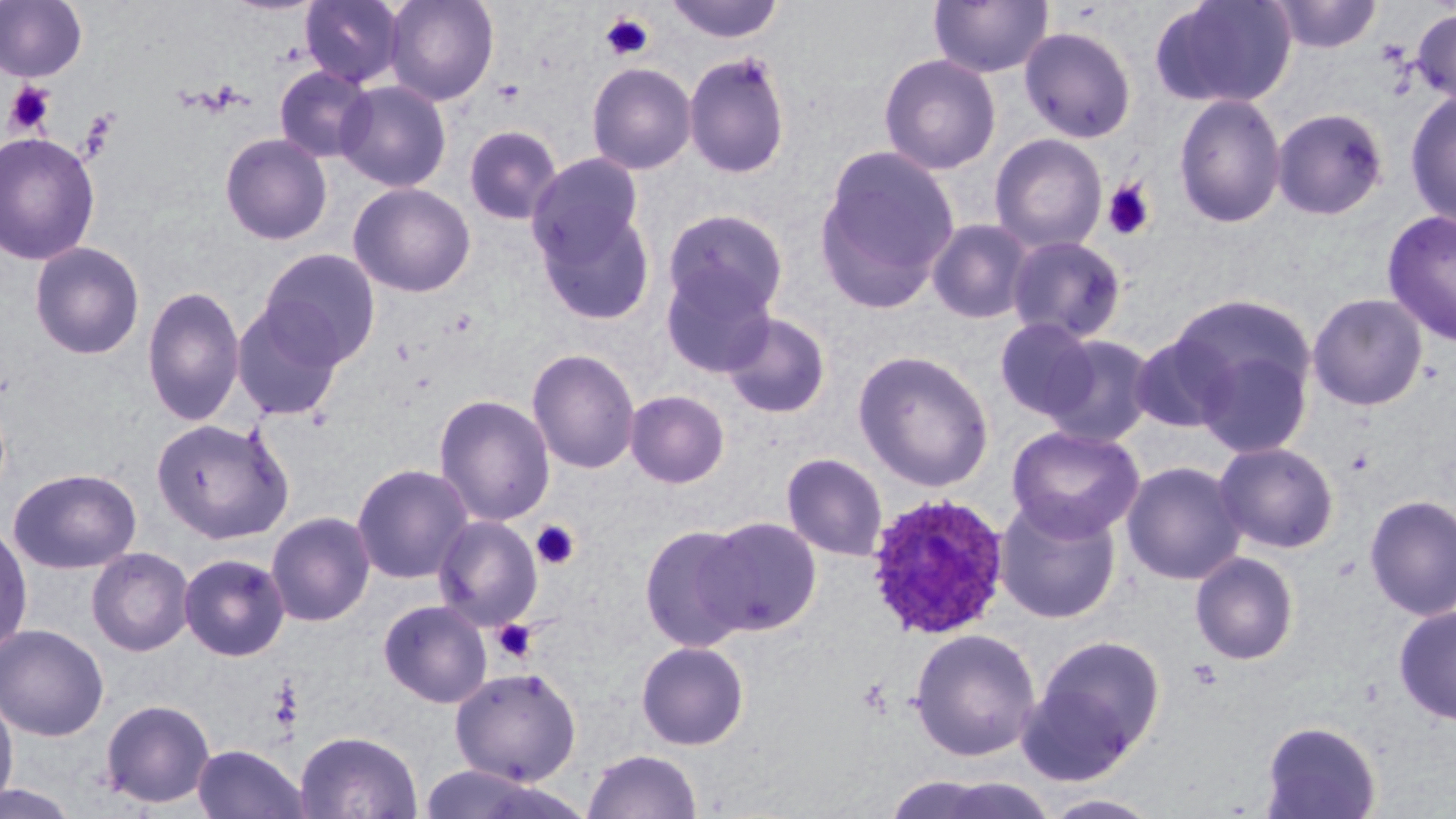

Approximate bounding boxes as (x1, y1, x2, y2) in pixels. Uninfected red blood cell locations: (300, 0, 405, 88), (384, 0, 499, 106), (664, 0, 785, 44), (1150, 0, 1298, 109), (0, 1, 88, 83), (928, 1, 1053, 79), (1268, 1, 1382, 53), (1411, 6, 1456, 105), (1019, 25, 1137, 143), (683, 51, 792, 179), (879, 53, 1001, 174), (586, 62, 696, 175), (274, 65, 376, 163), (335, 80, 452, 192), (1405, 90, 1456, 229), (1173, 93, 1286, 228), (1271, 108, 1389, 220), (463, 125, 563, 226), (0, 131, 101, 266), (219, 132, 332, 245), (989, 133, 1107, 253), (814, 147, 960, 312), (528, 153, 645, 266), (348, 182, 476, 297), (533, 201, 657, 324), (663, 208, 788, 319), (1382, 210, 1456, 347), (926, 219, 1035, 324), (1006, 235, 1127, 343), (29, 241, 145, 360), (258, 248, 382, 367), (660, 264, 778, 378), (141, 285, 246, 427), (1307, 293, 1429, 411), (1166, 294, 1318, 419), (231, 302, 345, 421), (720, 311, 831, 418), (993, 317, 1101, 422), (1129, 331, 1238, 434), (1039, 333, 1158, 447), (1192, 340, 1313, 459), (526, 348, 641, 474), (853, 350, 995, 492), (625, 389, 730, 488), (433, 394, 556, 526), (150, 417, 294, 544), (1006, 425, 1145, 542), (1213, 441, 1340, 553), (781, 452, 888, 562), (1121, 460, 1246, 585), (351, 463, 474, 584), (7, 467, 142, 574), (1363, 494, 1456, 620), (994, 496, 1123, 624), (266, 511, 377, 626), (433, 515, 543, 630), (699, 516, 823, 635), (0, 521, 34, 657), (638, 523, 757, 652), (86, 547, 195, 656), (178, 552, 290, 661), (1189, 552, 1300, 665), (378, 599, 492, 709), (1394, 605, 1456, 724), (0, 623, 110, 742), (909, 627, 1042, 762), (1029, 635, 1166, 768), (635, 641, 750, 751), (449, 666, 582, 785), (0, 691, 18, 812), (99, 698, 216, 808), (1260, 720, 1381, 819), (295, 730, 423, 818), (192, 744, 309, 819), (583, 749, 702, 819), (885, 772, 1053, 819), (0, 780, 82, 818), (1039, 792, 1165, 818). Platelet locations: (599, 12, 654, 62), (492, 78, 527, 106), (5, 82, 55, 136), (1101, 179, 1156, 241), (531, 520, 580, 570), (492, 619, 538, 663), (271, 677, 303, 732), (856, 678, 892, 716). Plasmodium ovale-infected red blood cell locations: (864, 492, 1011, 641). Slide-level diagnosis: Plasmodium ovale. 1000x magnification. Image is 1456×819 pixels. Single field of view. Thin blood smear. May-Grünwald-Giemsa stain. Light microscopy.